Assess the background quality.
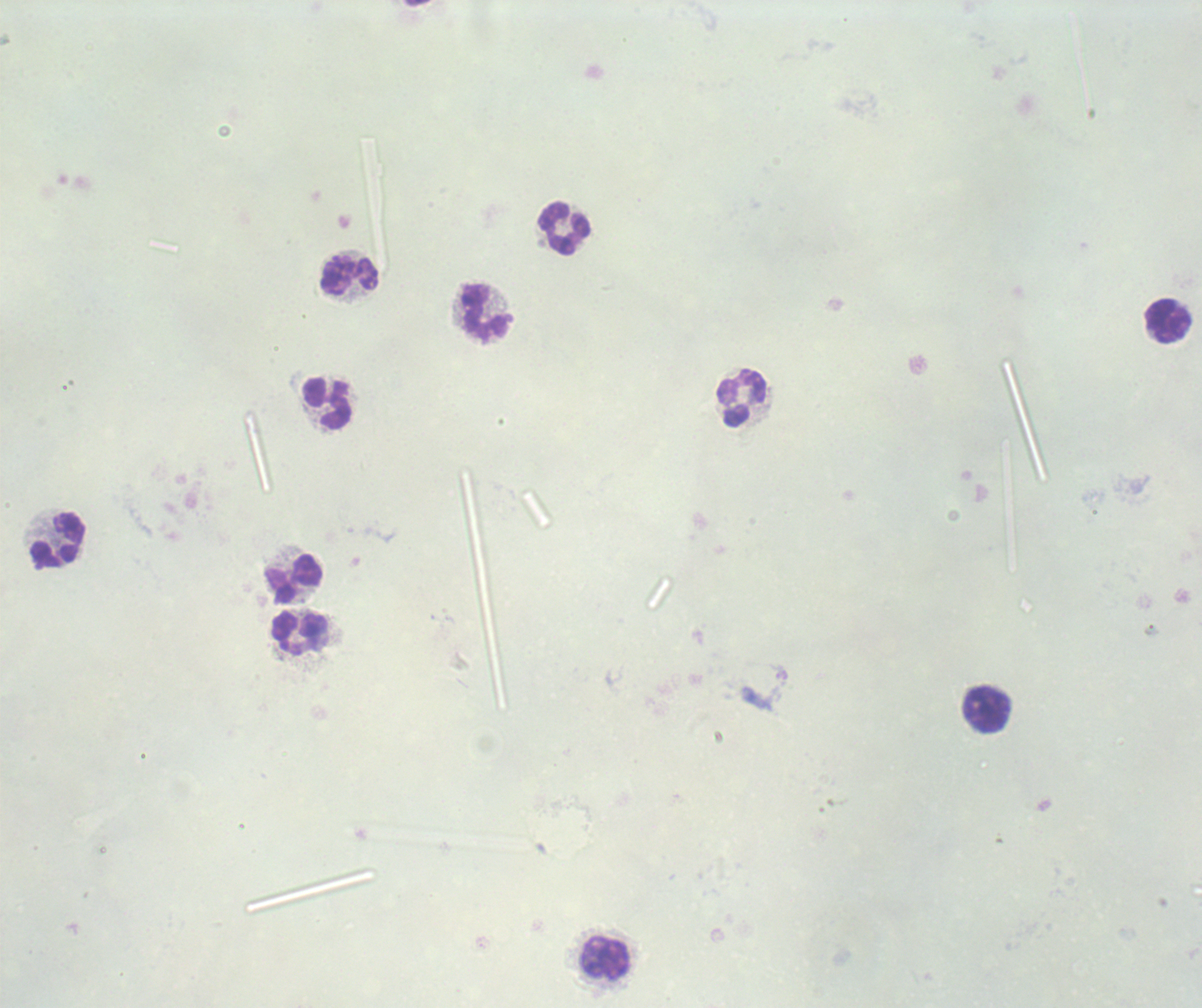
Satisfactory.

Approximate object centers, in pixels from the top-left corner. Leukocyte locations: (x=565, y=228), (x=350, y=276), (x=485, y=312), (x=1168, y=321), (x=741, y=398), (x=328, y=404), (x=59, y=540), (x=294, y=579), (x=300, y=634), (x=987, y=709), (x=606, y=958). Result: no Plasmodium parasites seen. Captured at 100x magnification. Previously used in an actual diagnosis. Romanowsky stain. Image is 1202×1008 pixels. Single field of view. Thick blood smear.